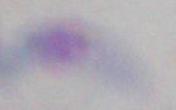
Photomicrograph. Toxoplasma gondii is seen. 1000x magnification.